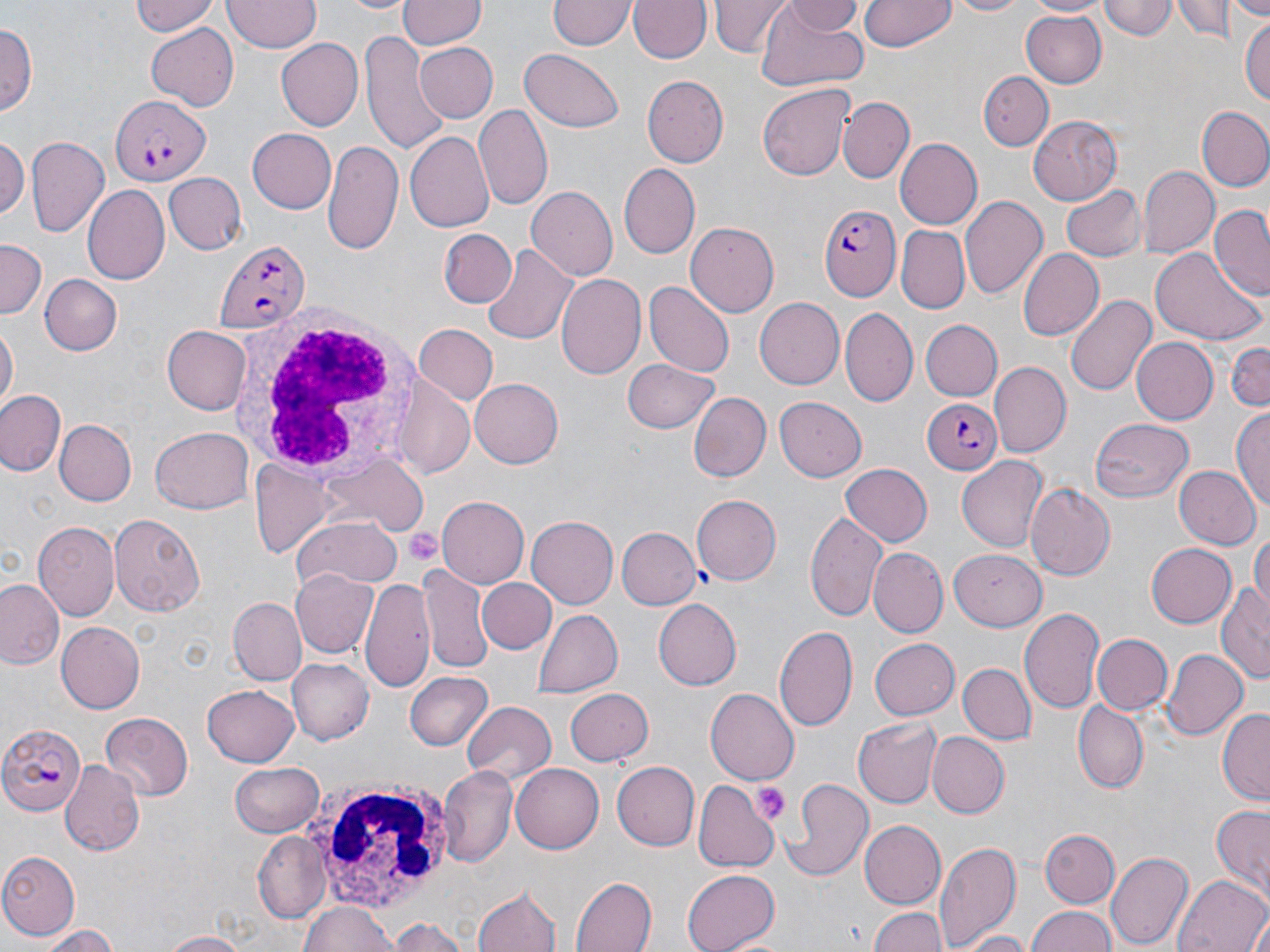
Approximate bounding boxes as (x1,y1)-(x2,y2) corner pairs in pixels. Uninfected red blood cell locations: (131,0)-(221,37), (224,0)-(318,54), (340,0)-(413,15), (398,0)-(484,50), (551,0)-(636,51), (629,0)-(713,64), (711,0)-(790,56), (779,0)-(862,37), (862,0)-(956,51), (943,0)-(1038,18), (1025,0)-(1111,17), (1102,0)-(1177,40), (1172,0)-(1238,44), (1231,0)-(1270,17), (754,2)-(871,91), (1018,11)-(1109,88), (1240,13)-(1270,111), (1,23)-(37,114), (145,23)-(241,110), (359,33)-(444,155), (278,38)-(363,131), (414,40)-(496,124), (517,49)-(627,133), (978,72)-(1052,148), (644,75)-(728,167), (758,85)-(855,181), (838,96)-(913,182), (474,104)-(554,211), (1196,105)-(1270,192), (1027,114)-(1123,204), (246,128)-(337,214), (405,133)-(494,234), (0,136)-(28,220), (26,136)-(108,236), (897,137)-(983,229), (323,139)-(402,254), (618,162)-(701,260), (1139,167)-(1218,259), (162,171)-(245,255), (1060,181)-(1144,264), (82,186)-(171,285), (527,187)-(621,280), (961,195)-(1048,302), (1209,205)-(1269,299), (685,222)-(780,316), (897,227)-(969,313), (439,230)-(513,309), (0,241)-(45,322), (482,242)-(578,344), (1150,245)-(1265,345), (1017,249)-(1103,342), (555,272)-(648,381), (41,275)-(121,355), (645,281)-(734,378), (1064,292)-(1157,400), (754,298)-(844,390), (840,307)-(917,406), (918,320)-(1002,402), (1,322)-(17,412), (165,324)-(251,414), (412,324)-(495,404), (1131,338)-(1218,425), (1226,340)-(1269,414), (621,358)-(722,436), (989,362)-(1070,456), (468,378)-(563,468), (398,385)-(472,478), (1,390)-(67,476), (690,392)-(772,484), (774,397)-(866,482), (1232,405)-(1270,513), (1089,418)-(1195,502), (56,421)-(136,506), (150,427)-(252,513), (957,456)-(1050,551), (838,463)-(931,546), (1172,465)-(1259,550), (1025,484)-(1115,582), (691,493)-(782,585), (437,497)-(528,588), (804,509)-(888,621), (110,513)-(208,617), (528,515)-(622,608), (292,516)-(403,594), (34,523)-(119,620), (403,524)-(443,569), (615,525)-(701,608), (1251,528)-(1270,610), (1146,543)-(1236,626), (948,547)-(1045,630), (870,548)-(947,637), (417,560)-(492,672), (290,567)-(381,660), (477,576)-(556,653), (360,577)-(434,694), (0,579)-(65,670), (1217,587)-(1269,682), (229,596)-(305,686), (653,598)-(744,689), (1020,608)-(1104,716), (532,609)-(622,697), (57,621)-(145,713), (775,624)-(858,734), (1092,634)-(1174,715), (867,637)-(959,721), (1161,647)-(1247,742), (288,658)-(375,744), (959,663)-(1033,743), (404,671)-(494,753), (201,685)-(301,767), (564,688)-(654,768), (706,689)-(798,782), (462,702)-(558,780), (1074,703)-(1149,793), (1217,708)-(1270,807), (99,711)-(194,802), (854,717)-(941,805), (927,732)-(1009,817), (60,761)-(144,856), (231,761)-(326,836), (613,762)-(699,851), (439,764)-(517,866), (511,765)-(604,852), (782,777)-(873,881), (693,782)-(779,869), (1210,805)-(1270,901), (856,819)-(946,910), (1040,828)-(1119,907), (252,832)-(332,923), (935,839)-(1022,952), (1107,850)-(1193,951), (0,851)-(81,939), (681,869)-(781,952), (1172,875)-(1270,952), (570,876)-(655,952), (473,883)-(562,952), (298,899)-(403,952), (868,907)-(948,952), (1026,907)-(1119,952), (387,917)-(473,952), (31,926)-(122,951), (156,931)-(250,951), (957,932)-(1035,952). Plasmodium falciparum-infected red blood cell locations: (113,93)-(209,188), (820,202)-(900,303), (214,241)-(311,332), (918,398)-(1003,475), (0,722)-(84,815). Platelet locations: (403,527)-(444,564), (753,782)-(790,824). White blood cell locations: (227,303)-(425,484), (308,776)-(456,913). Slide-level diagnosis: Plasmodium falciparum. Thin blood smear. May-Grünwald-Giemsa stain. One field of a larger specimen. Image is 1270×952 pixels. Captured at 1000x magnification. Optical microscopy.